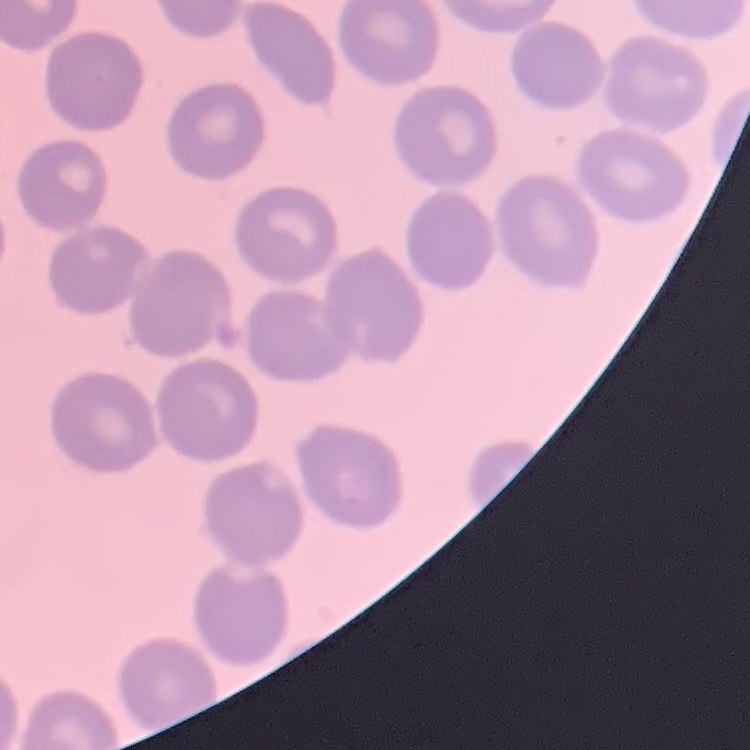

The erythrocytes show no rouleaux formation. Square crop of a larger photomicrograph. Thin peripheral smear. Stained with either Field's or Giemsa.